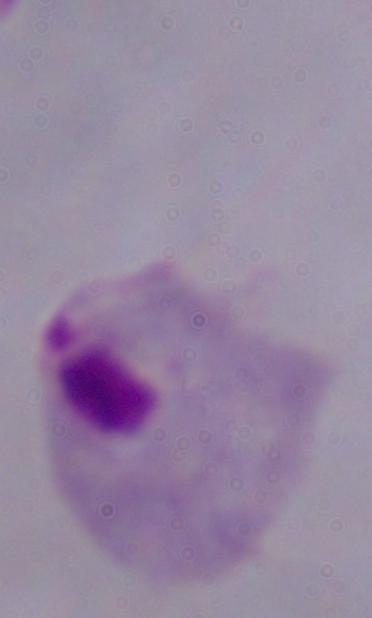
Summary:
  - Identification: trichomonad
  - Modality: photomicrograph
  - Magnification: 1000x